Assess this cell for malaria.
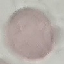
Uninfected.

stain = Giemsa
image type = automatically extracted cell patch, resized to 64 × 64 pixels
capture = smartphone camera at the microscope eyepiece
preparation = thin smear